Identify the cell.
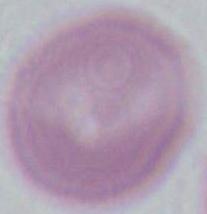
An erythrocyte.

Summary:
  - Modality: photomicrograph
  - Magnification: 1000x